State the preparation type.
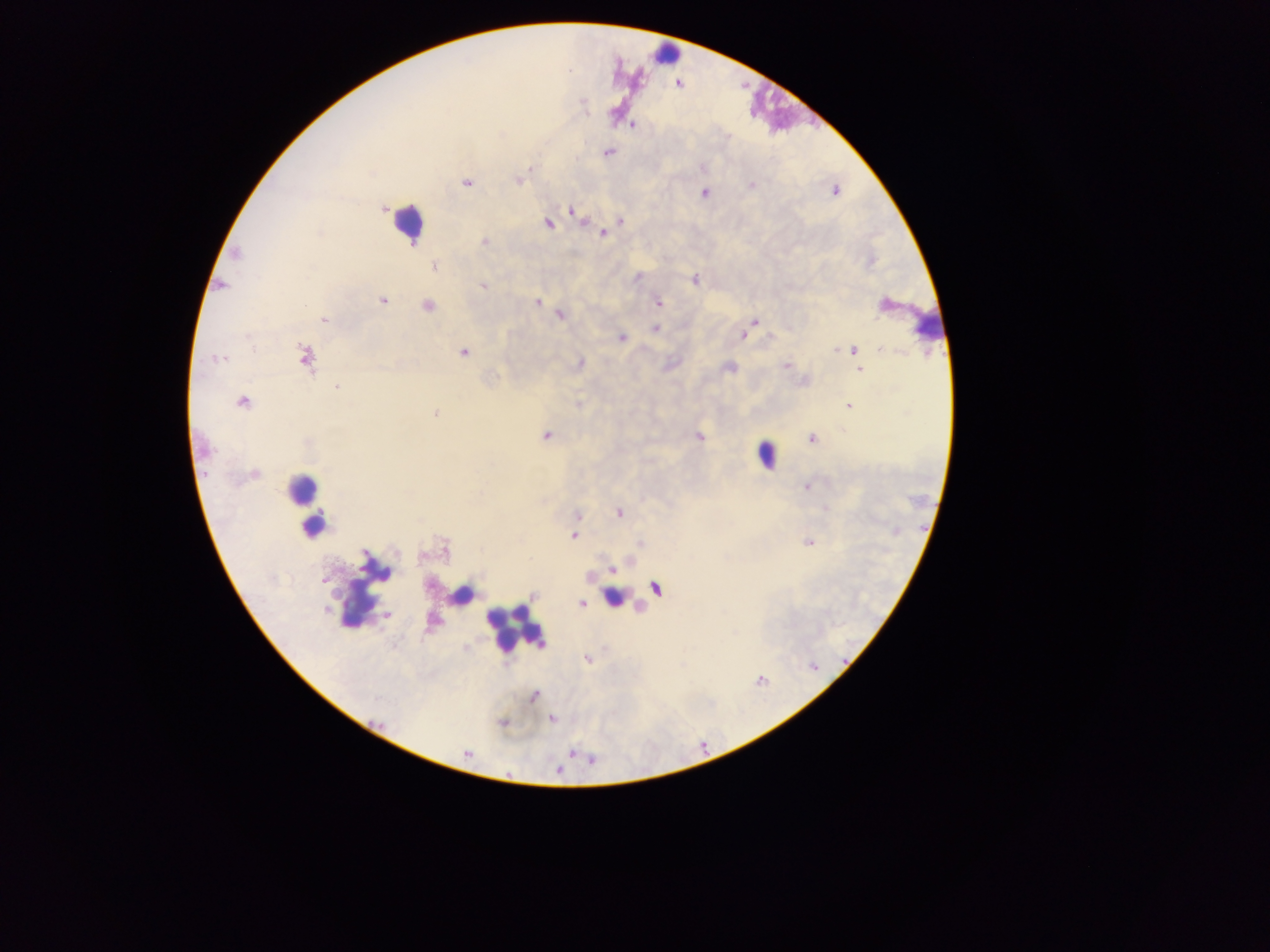

This is a thick smear.

Approximate centers as x y in pixels.
Summary:
  - Plasmodium parasite locations: 633 125; 608 152; 519 180; 466 183; 703 192; 835 192; 572 211; 621 220; 548 224; 603 234; 484 242; 237 253; 434 266; 637 278; 694 280; 482 286; 382 301; 537 303; 658 303; 426 306; 560 315; 324 319; 755 322; 655 329; 743 335; 621 337; 852 350; 463 353; 304 357; 218 358; 786 365; 729 368; 859 370; 337 387; 242 402; 848 406; 436 413; 545 436; 699 437; 812 439; 806 487; 618 512; 576 515; 574 536; 808 542; 323 580; 656 588; 533 594; 582 604; 387 614; 587 659; 535 697; 551 719; 502 723
  - Leukocyte locations: 665 54; 406 222; 927 319; 765 456; 306 493; 314 526; 362 588; 460 594; 614 597; 513 628
  - Field of view: single
  - Image size: 1270×952 pixels
  - Capture: mobile-phone photograph through a microscope
  - Country: Ghana